Name the parasite shown.
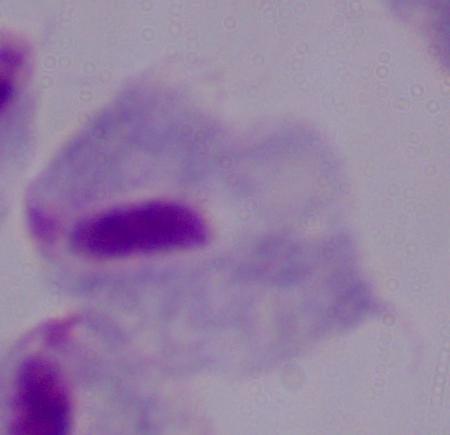

A trichomonad.

Summary:
  - Modality: photomicrograph
  - Magnification: 1000x